Identify the parasite.
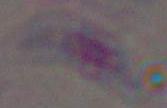

This is Toxoplasma gondii.

modality = micrograph
magnification = 1000x